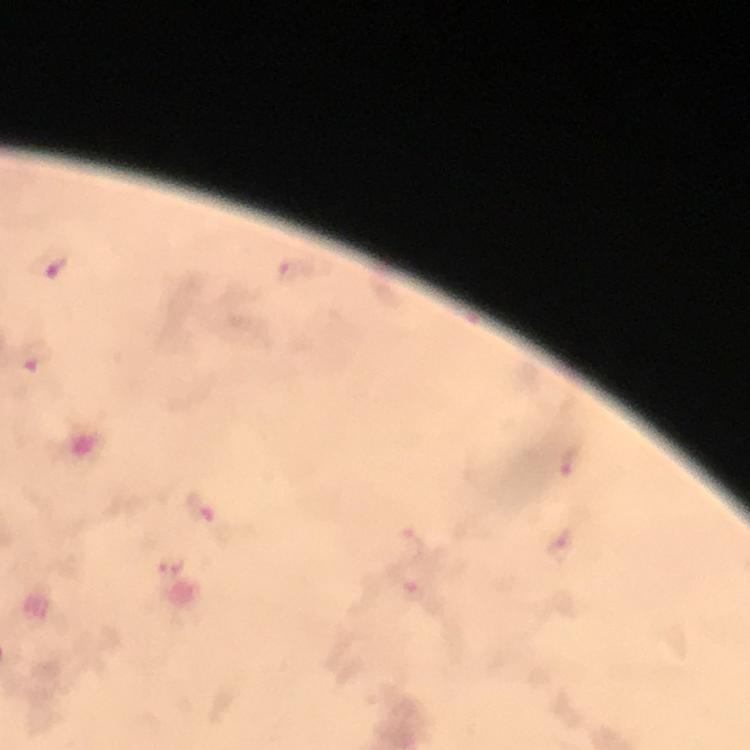
{
  "cropped_from": "one field of view",
  "plasmodium_parasite_locations": "approximate centers as (x, y) in pixels: (50, 263), (287, 272), (37, 355), (570, 464), (200, 510), (410, 543), (559, 545), (173, 564), (410, 590)",
  "capture": "smartphone mounted on the microscope",
  "context": "from a malaria diagnostic workup",
  "image_size": "750×750 pixels",
  "stain": "Giemsa",
  "magnification": "100x",
  "immersion_oil": "applied",
  "preparation": "thick smear"
}